Outline each blood parasite and name the species.
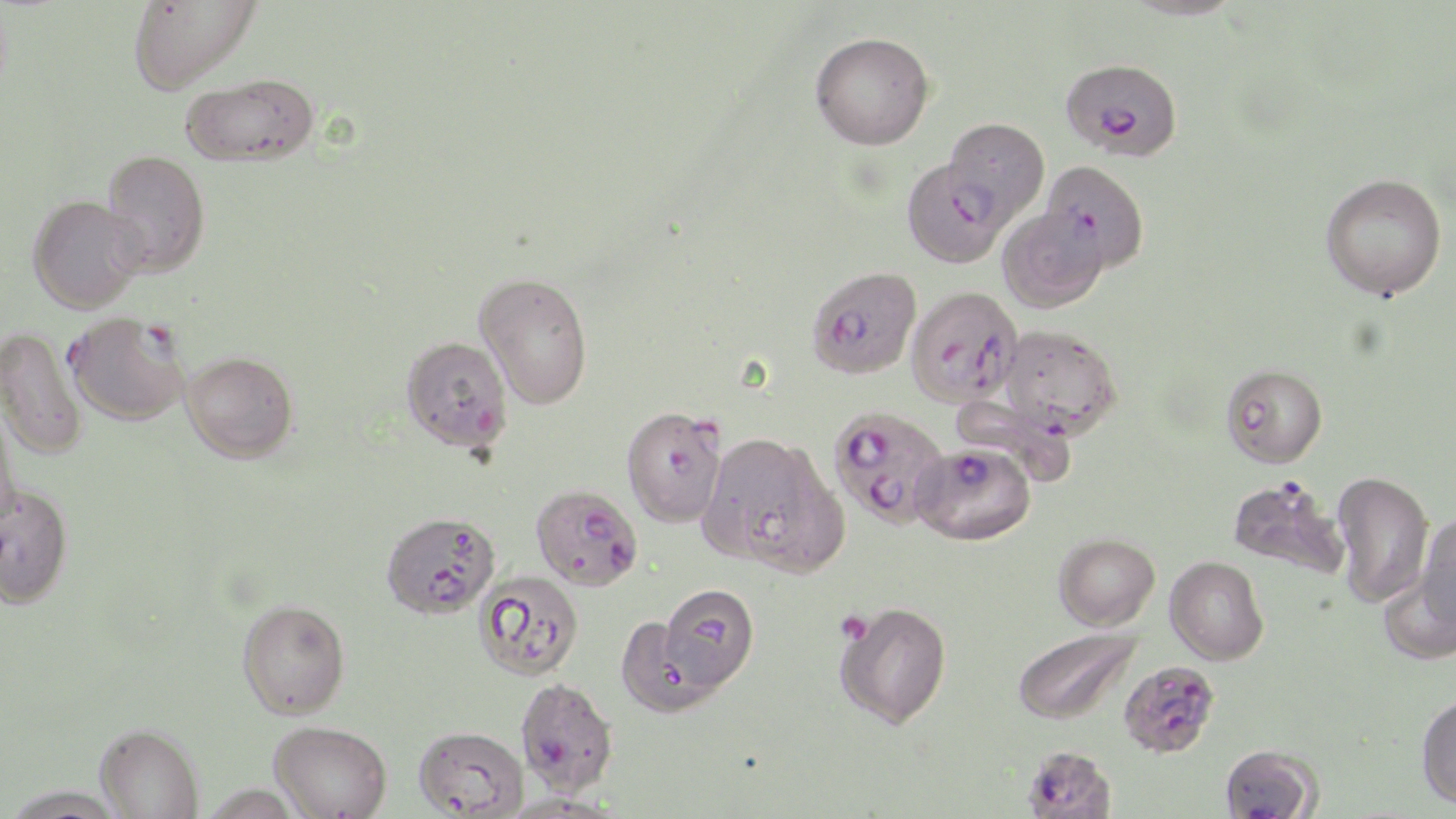
Approximate bounding boxes as [x1, y1, x2, y2] in pixels.
Plasmodium falciparum-infected red blood cells: [1061, 58, 1182, 161], [943, 118, 1050, 226], [998, 207, 1108, 313], [806, 266, 921, 379], [905, 285, 1023, 407], [65, 312, 189, 426], [401, 336, 513, 452], [621, 405, 727, 527], [828, 405, 950, 528], [911, 442, 1035, 545], [1228, 475, 1348, 578], [531, 484, 643, 591], [381, 511, 500, 618], [474, 570, 584, 681], [1118, 660, 1220, 758], [515, 677, 620, 797], [1219, 743, 1322, 819], [1023, 745, 1116, 819].
No Plasmodium ovale, Plasmodium malariae, Plasmodium vivax, Babesia divergens, or Trypanosoma brucei observed.

Platelet locations: [842, 616, 868, 644]. Uninfected red blood cell locations: [126, 0, 260, 93], [1121, 0, 1245, 21], [810, 31, 935, 150], [180, 74, 320, 166], [101, 150, 211, 276], [901, 159, 1009, 268], [1040, 159, 1149, 275], [1320, 172, 1447, 300], [27, 195, 145, 313], [474, 272, 593, 409], [999, 325, 1122, 437], [0, 326, 88, 460], [182, 351, 298, 463], [1221, 364, 1328, 468], [949, 393, 1079, 487], [0, 396, 17, 526], [700, 431, 845, 574], [1331, 470, 1433, 608], [0, 480, 73, 607], [1415, 512, 1456, 630], [1053, 532, 1160, 631], [1168, 562, 1269, 665], [1379, 571, 1456, 666], [658, 582, 759, 691], [236, 599, 350, 719], [834, 600, 952, 729], [615, 615, 725, 718], [1012, 626, 1143, 725], [1416, 691, 1456, 809], [269, 720, 391, 819], [95, 723, 204, 819], [413, 725, 529, 817], [2, 784, 127, 818], [500, 793, 622, 819]. Slide-level diagnosis: Plasmodium falciparum. Thin blood smear. Optical microscopy. Image is 1456×819 pixels. May-Grünwald-Giemsa-stained preparation. Single field of view. Captured at 1000x magnification.